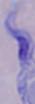

1000x magnification. Micrograph. A trypanosome is seen.